Describe the morphology of the erythrocytes.
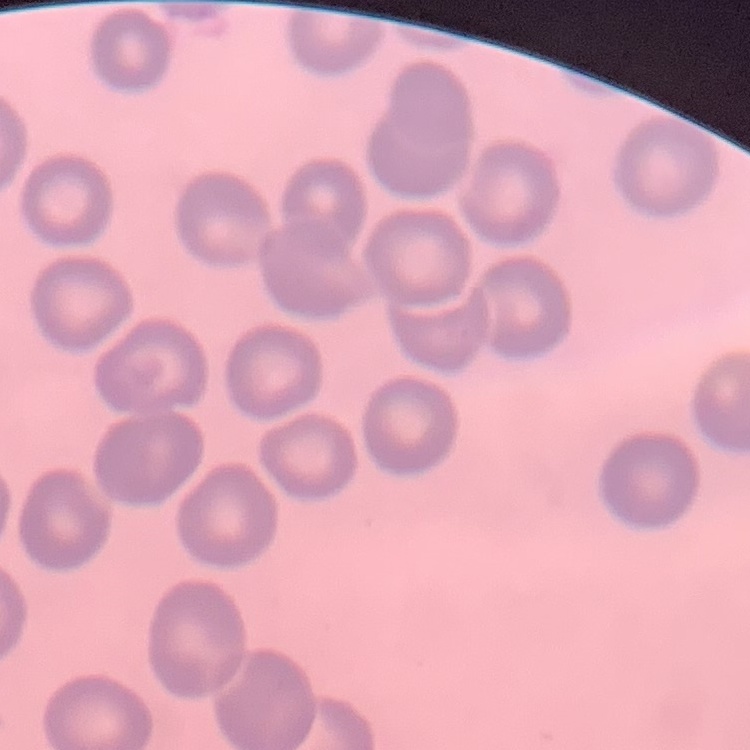
No rouleaux formation.

Summary:
  - Stain: Field's or Giemsa
  - Image type: one tile cut from a larger photomicrograph
  - Preparation: thin blood smear